Outline platelets.
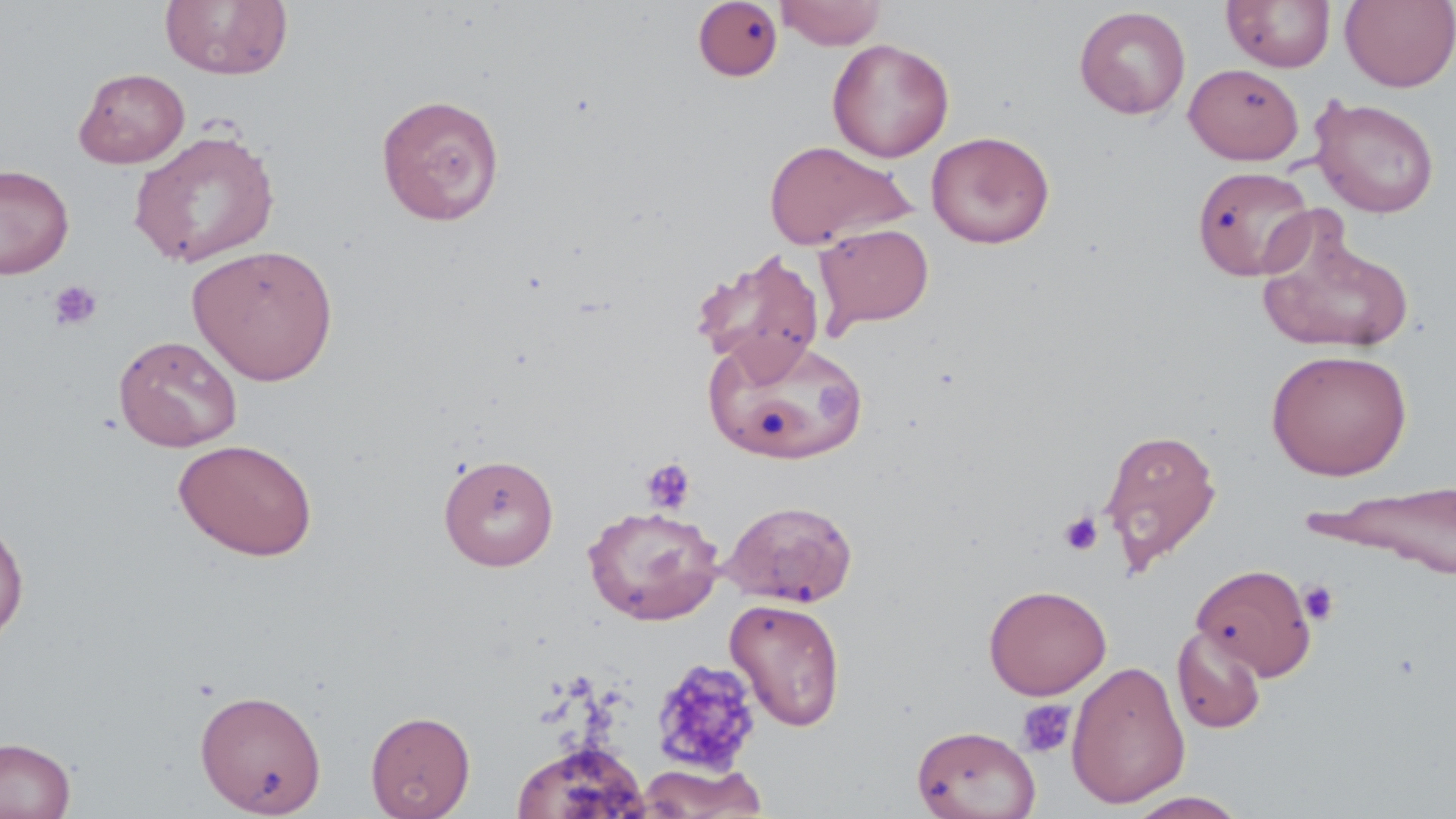
Approximate bounding boxes as named x1/y1/x2/y2 corners in pixels.
Platelets: (x1=47, y1=279, x2=104, y2=332), (x1=641, y1=457, x2=696, y2=515), (x1=1059, y1=511, x2=1104, y2=556), (x1=1298, y1=580, x2=1340, y2=626), (x1=649, y1=656, x2=764, y2=777), (x1=1017, y1=698, x2=1076, y2=758).

slide_level_diagnosis: no evidence of blood parasites
modality: optical microscopy
image_size: 1456×819 pixels
preparation: thin blood smear
stain: May-Grünwald-Giemsa
field_of_view: single
uninfected_red_blood_cell_locations: 'approximate bounding boxes as named x1/y1/x2/y2 corners in pixels: (x1=775, y1=0, x2=887, y2=49), (x1=1222, y1=0, x2=1336, y2=73), (x1=1340, y1=0, x2=1456, y2=91), (x1=160, y1=1, x2=293, y2=81), (x1=692, y1=1, x2=783, y2=81), (x1=1074, y1=6, x2=1191, y2=119), (x1=827, y1=38, x2=954, y2=162), (x1=1183, y1=62, x2=1304, y2=164), (x1=74, y1=67, x2=190, y2=168), (x1=375, y1=92, x2=506, y2=225), (x1=1310, y1=96, x2=1440, y2=218), (x1=129, y1=129, x2=280, y2=268), (x1=926, y1=131, x2=1054, y2=248), (x1=763, y1=140, x2=912, y2=251), (x1=0, y1=164, x2=74, y2=279), (x1=1192, y1=165, x2=1316, y2=282), (x1=1257, y1=220, x2=1417, y2=355), (x1=814, y1=223, x2=934, y2=333), (x1=187, y1=243, x2=339, y2=386), (x1=692, y1=249, x2=826, y2=378), (x1=704, y1=333, x2=865, y2=466), (x1=113, y1=334, x2=242, y2=452), (x1=1266, y1=348, x2=1413, y2=480), (x1=1099, y1=426, x2=1221, y2=573), (x1=173, y1=438, x2=318, y2=561), (x1=438, y1=454, x2=559, y2=572), (x1=1308, y1=480, x2=1456, y2=578), (x1=721, y1=498, x2=858, y2=608), (x1=583, y1=504, x2=724, y2=626), (x1=0, y1=512, x2=30, y2=653), (x1=1192, y1=562, x2=1318, y2=680), (x1=984, y1=583, x2=1111, y2=700), (x1=725, y1=598, x2=847, y2=731), (x1=1172, y1=625, x2=1267, y2=734), (x1=1067, y1=660, x2=1190, y2=808), (x1=194, y1=688, x2=327, y2=817), (x1=365, y1=710, x2=476, y2=819), (x1=912, y1=724, x2=1041, y2=819), (x1=0, y1=735, x2=76, y2=819), (x1=511, y1=740, x2=650, y2=819), (x1=635, y1=762, x2=769, y2=818), (x1=1124, y1=791, x2=1249, y2=818)'
magnification: 1000x